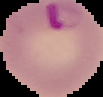

Summary:
  - Malaria status: parasitized
  - Image size: 103×97 pixels
  - Preparation: thin blood film
  - Image type: segmented cell region with the area outside set to black